Name the parasite shown.
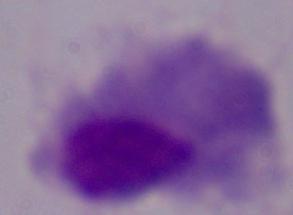
A trichomonad.

magnification = 1000x
modality = photomicrograph